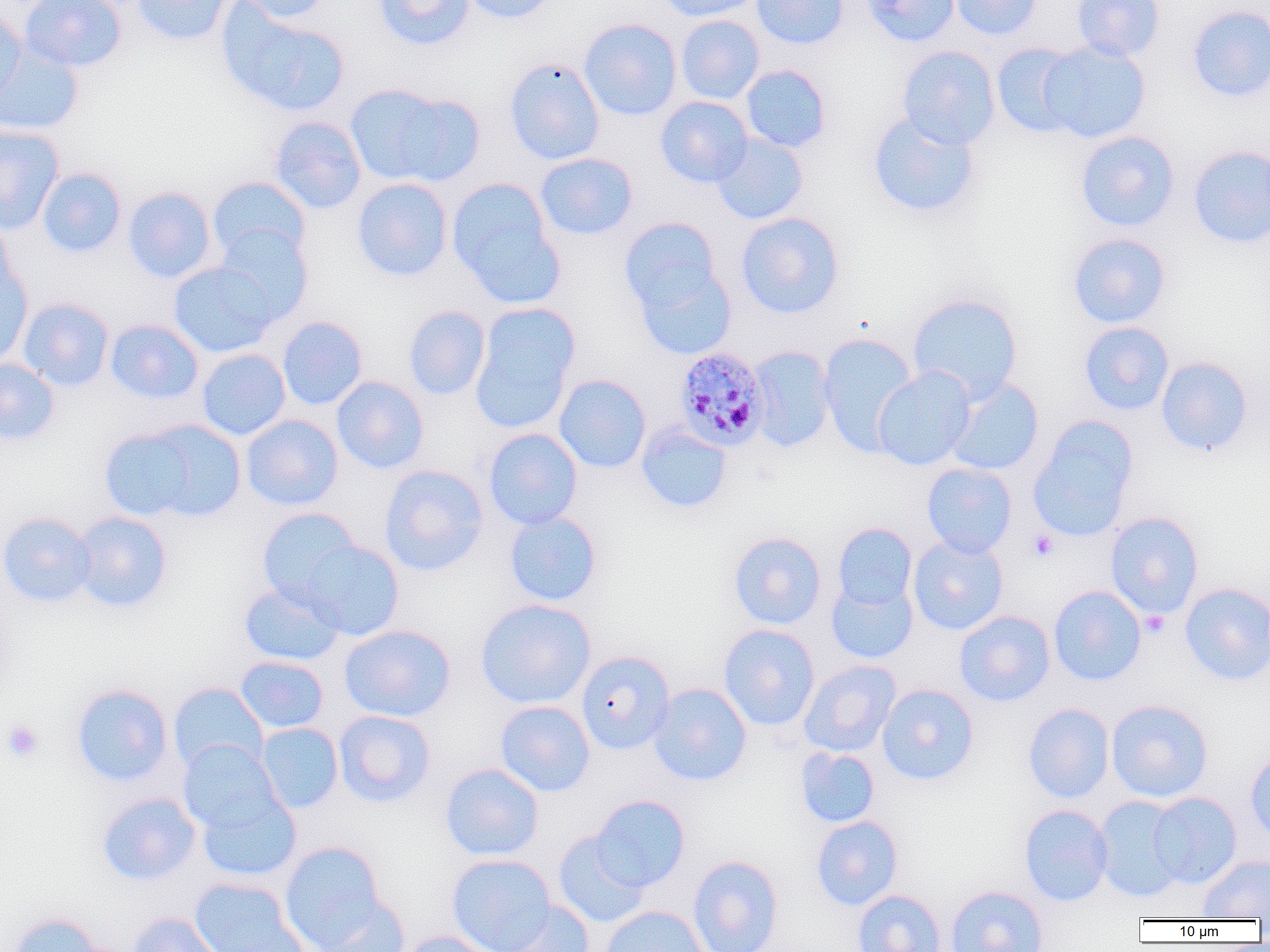
Approximate bounding boxes as [x1, y1, x2, y2] in pixels. Uninfected red blood cell locations: [19, 0, 127, 71], [131, 0, 235, 46], [234, 0, 333, 23], [374, 0, 475, 50], [462, 0, 558, 24], [656, 0, 763, 21], [751, 0, 849, 49], [862, 0, 959, 46], [949, 0, 1042, 40], [1072, 0, 1164, 61], [218, 4, 351, 117], [1186, 5, 1270, 103], [0, 7, 26, 104], [676, 15, 764, 104], [579, 18, 682, 121], [1038, 41, 1151, 143], [0, 42, 84, 136], [991, 42, 1085, 137], [897, 45, 1000, 149], [503, 57, 605, 165], [740, 65, 831, 153], [344, 84, 470, 187], [655, 96, 753, 188], [867, 109, 981, 219], [268, 116, 366, 214], [0, 125, 65, 235], [1075, 131, 1180, 232], [712, 133, 808, 224], [1188, 144, 1270, 249], [535, 153, 637, 240], [37, 167, 126, 258], [208, 176, 311, 265], [352, 178, 453, 282], [446, 178, 564, 307], [122, 186, 217, 283], [736, 212, 844, 318], [0, 215, 17, 303], [619, 216, 723, 316], [215, 225, 313, 324], [1068, 233, 1170, 328], [168, 261, 278, 357], [0, 262, 33, 367], [635, 263, 737, 361], [908, 293, 1023, 402], [18, 298, 114, 392], [403, 306, 490, 400], [470, 308, 578, 434], [277, 316, 368, 410], [105, 319, 204, 405], [1079, 322, 1174, 416], [818, 332, 919, 456], [745, 345, 837, 452], [196, 349, 291, 440], [1156, 356, 1253, 457], [0, 358, 60, 447], [872, 365, 976, 471], [554, 374, 651, 473], [331, 376, 429, 474], [944, 377, 1044, 476], [241, 414, 343, 510], [1027, 416, 1138, 541], [101, 421, 244, 521], [636, 423, 732, 513], [483, 428, 583, 530], [921, 463, 1017, 557], [379, 464, 489, 576], [256, 507, 362, 607], [71, 511, 173, 613], [504, 511, 602, 606], [1105, 511, 1204, 619], [0, 512, 96, 607], [832, 522, 917, 611], [728, 532, 827, 629], [908, 535, 1008, 636], [299, 539, 405, 641], [826, 577, 919, 664], [239, 580, 344, 665], [1179, 582, 1270, 685], [1048, 585, 1146, 686], [475, 598, 596, 709], [954, 610, 1055, 706], [339, 624, 456, 722], [719, 624, 820, 731], [576, 651, 675, 754], [235, 656, 329, 733], [799, 660, 900, 756], [168, 682, 268, 775], [70, 683, 174, 787], [648, 683, 752, 786], [877, 683, 979, 785], [1106, 698, 1213, 802], [495, 701, 595, 797], [1023, 703, 1114, 803], [333, 710, 435, 807], [256, 722, 343, 813], [177, 740, 283, 835], [796, 747, 879, 827], [1245, 747, 1270, 844], [440, 763, 544, 861], [195, 790, 301, 883], [96, 792, 201, 886], [1148, 792, 1242, 888], [590, 794, 690, 891], [1092, 795, 1189, 903], [1018, 804, 1114, 906], [810, 816, 903, 910], [553, 831, 651, 927], [279, 840, 386, 950], [447, 854, 556, 952], [1197, 854, 1270, 920], [688, 855, 784, 952], [188, 877, 303, 952], [945, 885, 1048, 952], [852, 890, 946, 952], [310, 894, 411, 952], [494, 899, 595, 952], [598, 905, 712, 952], [6, 912, 105, 952], [126, 912, 225, 952], [398, 931, 501, 952]. Platelet locations: [1028, 529, 1058, 561], [1140, 610, 1170, 638], [2, 720, 44, 763]. Plasmodium malariae-infected red blood cell locations: [674, 346, 769, 452]. Slide-level diagnosis: Plasmodium malariae. Thin blood film. One field of a larger specimen. Captured at 1000x magnification. Optical microscopy. Image is 1270×952 pixels.